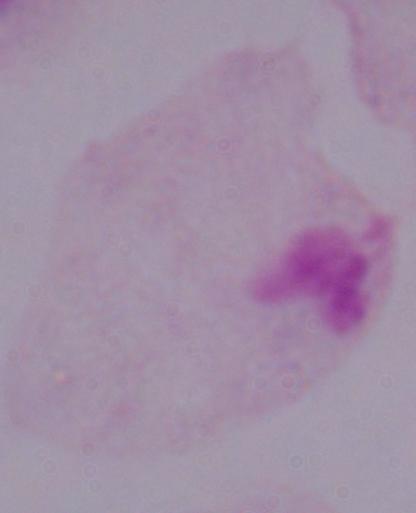

Summary:
  - Modality: photomicrograph
  - Magnification: 1000x
  - Identification: trichomonad